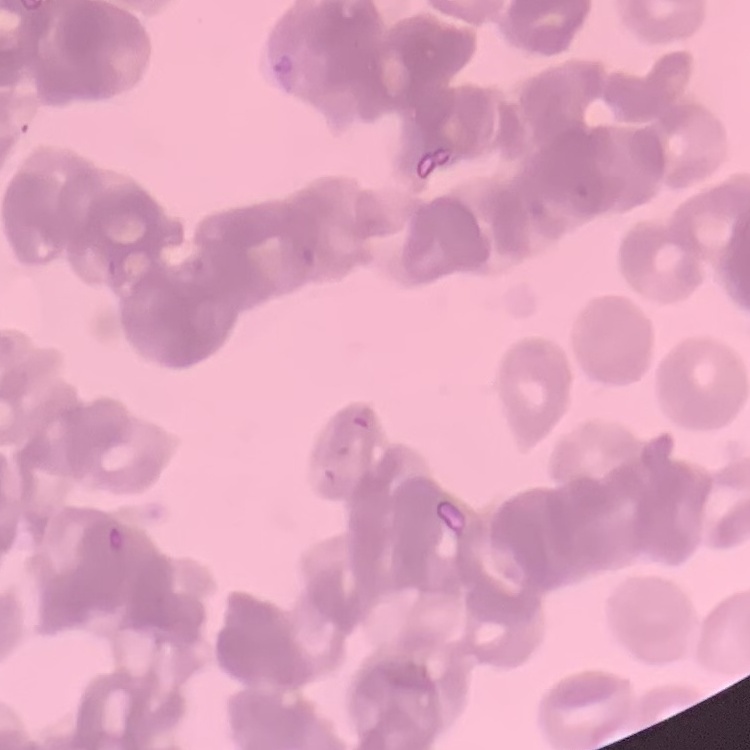
Summary:
  - Red blood cell morphology: rouleaux formation
  - Image type: one tile cut from a larger photomicrograph
  - Stain: Field's or Giemsa
  - Preparation: thin blood smear